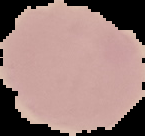
Malaria status: uninfected. From a thin blood smear. Image is 145×136 pixels. Cell region segmented out of the field of view; the surrounding area is masked to black.